Describe the morphology of the erythrocytes.
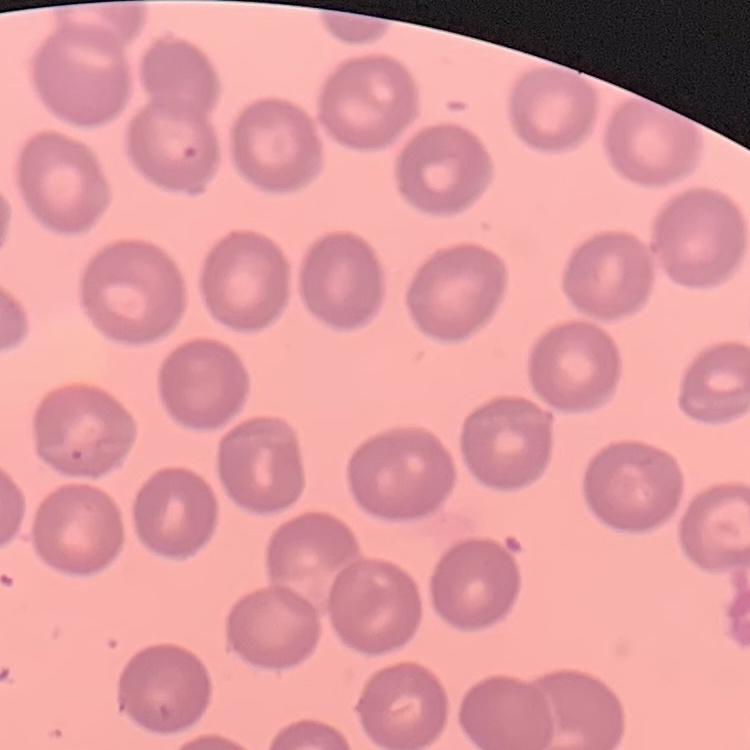

They show no rouleaux formation.

image type = one tile cut from a larger photomicrograph
preparation = thin peripheral smear
stain = Field's or Giemsa